Point out every Plasmodium parasite and every leukocyte.
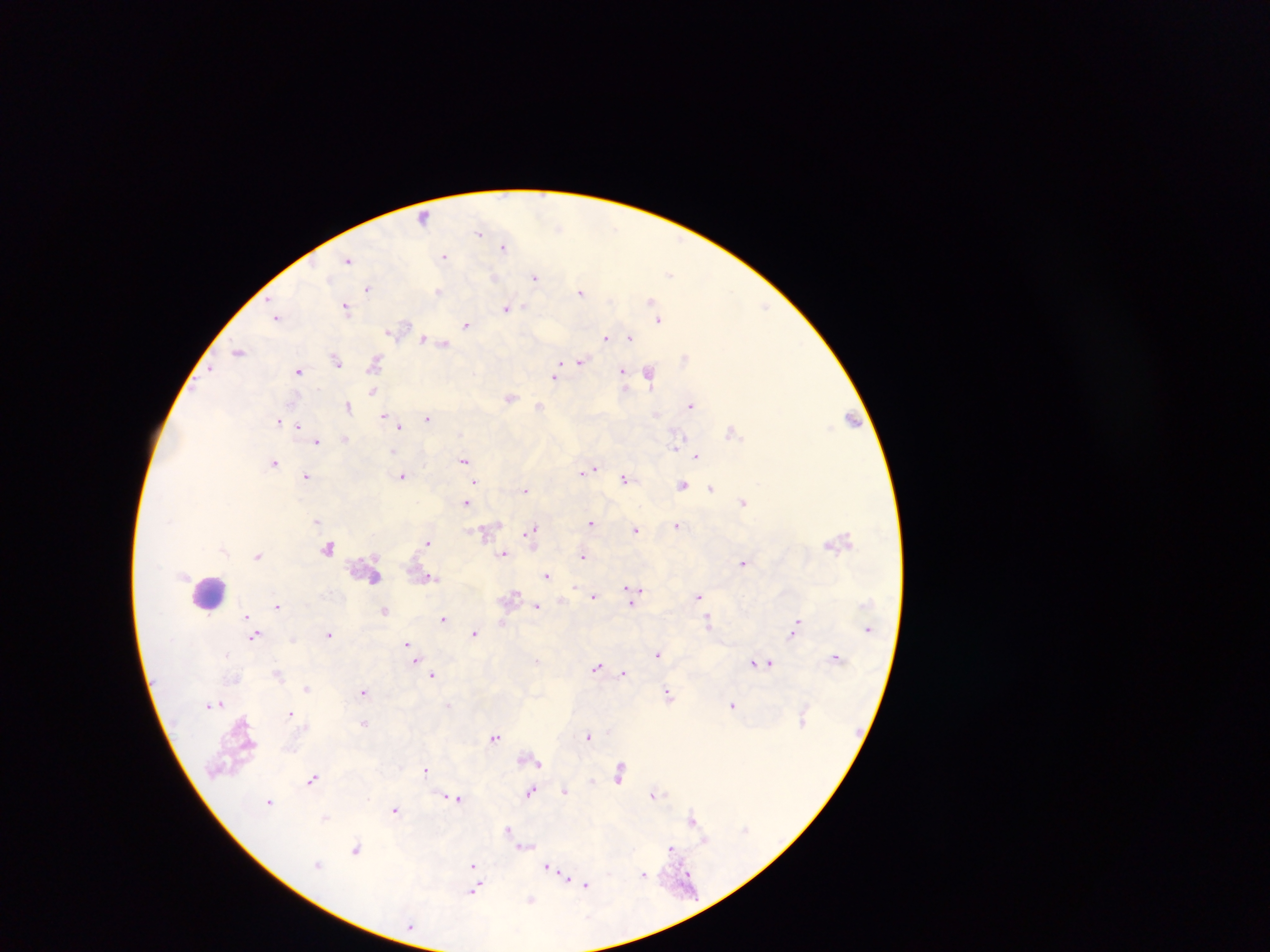

Approximate centers as x y in pixels.
Plasmodium parasites: 424 218; 480 232; 505 246; 444 256; 348 259; 671 272; 495 276; 535 277; 369 288; 438 290; 581 292; 653 302; 346 306; 507 308; 657 315; 277 317; 659 319; 467 323; 391 331; 608 336; 630 336; 424 338; 443 344; 239 351; 685 358; 336 359; 560 361; 581 361; 375 362; 212 369; 299 370; 623 370; 650 372; 556 375; 373 391; 510 398; 348 405; 691 405; 540 406; 384 416; 428 417; 853 418; 279 420; 285 423; 395 423; 298 424; 400 426; 733 432; 345 439; 317 440; 677 446; 696 455; 464 460; 274 462; 588 469; 307 476; 403 476; 625 478; 474 482; 683 485; 712 487; 525 488; 743 501; 466 502; 317 520; 592 522; 678 525; 636 530; 488 531; 531 531; 428 542; 330 549; 504 552; 258 555; 583 555; 744 562; 546 575; 430 577; 635 592; 593 596; 699 596; 632 599; 277 605; 537 606; 384 610; 247 615; 444 618; 709 622; 502 623; 795 627; 474 633; 329 634; 254 635; 407 645; 658 653; 226 654; 837 657; 416 661; 537 661; 753 662; 770 662; 597 667; 278 673; 623 673; 433 675; 307 686; 364 691; 668 693; 220 703; 449 704; 734 705; 290 712; 364 723; 495 736; 589 736; 535 759; 426 770; 620 772; 313 778; 593 782; 565 790; 531 791; 655 793; 456 798; 270 801; 395 810; 325 817; 693 819; 508 829; 705 840; 525 846; 671 848; 356 850; 319 864; 548 866; 473 867; 554 872; 644 874; 687 876; 474 879; 568 879; 585 885; 474 890; 531 900.
Leukocytes: 210 591; 232 749.

{
  "country": "Ghana",
  "preparation": "thick blood film",
  "image_size": "1270×952 pixels",
  "capture": "mobile-phone photograph through a microscope",
  "field_of_view": "single"
}